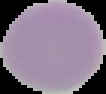 Malaria status: uninfected. Cell region segmented out of the field of view; the surrounding area is masked to black. From a thin blood film. Image is 106×94 pixels.